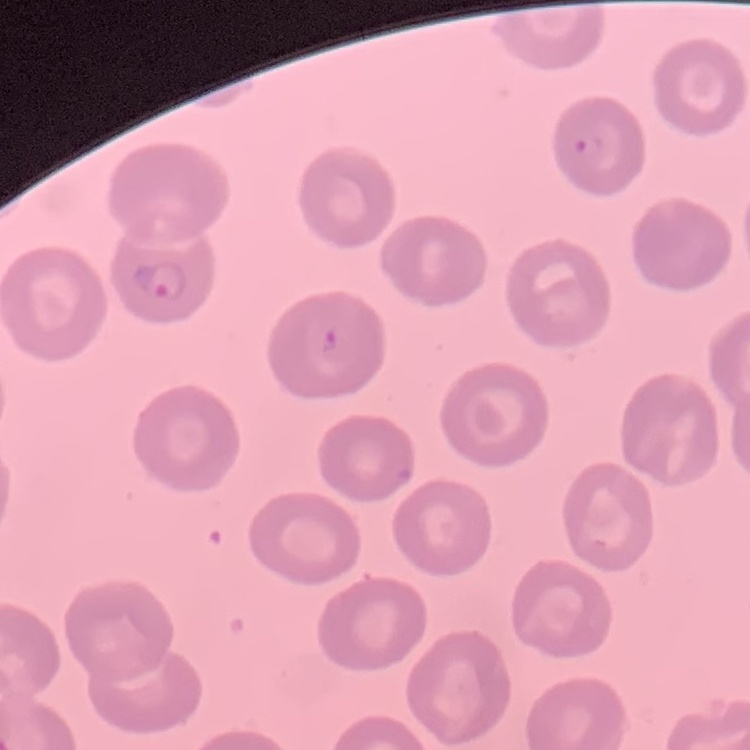

Summary:
  - Erythrocyte morphology: no rouleaux formation
  - Stain: Field's or Giemsa
  - Preparation: thin blood smear
  - Image type: one tile cut from a larger photomicrograph